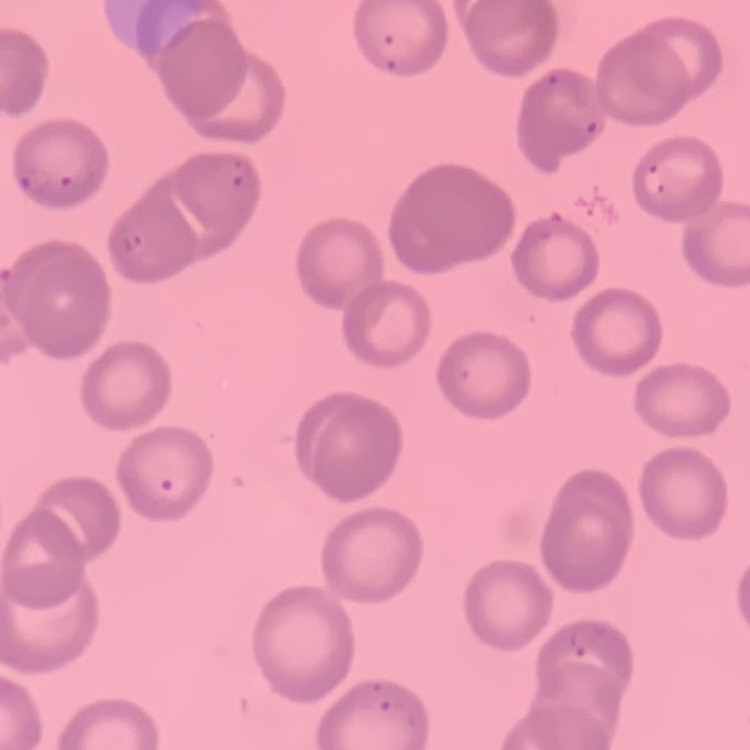 The erythrocytes exhibit no rouleaux formation. Field's or Giemsa stain. Thin blood film. Square crop of a larger photomicrograph.